State the blood parasite species.
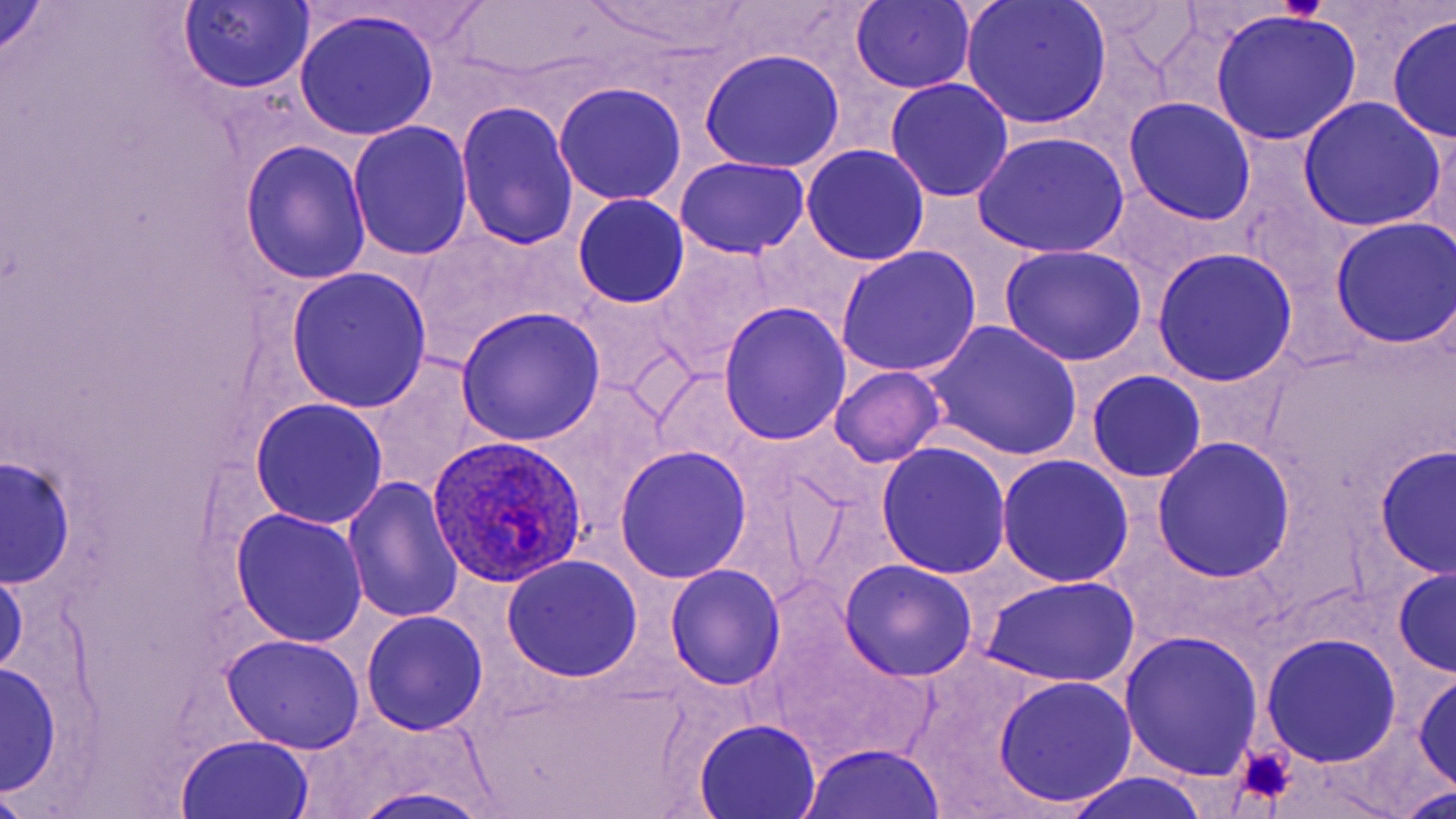

Plasmodium ovale.

Summary:
  - Coordinate format: approximate bounding boxes as named x1/y1/x2/y2 corners in pixels
  - Platelet locations: (x1=1278, y1=0, x2=1326, y2=23), (x1=1230, y1=743, x2=1299, y2=809)
  - Plasmodium ovale-infected red blood cell locations: (x1=426, y1=431, x2=589, y2=583)
  - Uninfected red blood cell locations: (x1=959, y1=0, x2=1111, y2=129), (x1=0, y1=1, x2=52, y2=65), (x1=850, y1=2, x2=975, y2=94), (x1=177, y1=3, x2=314, y2=92), (x1=295, y1=10, x2=440, y2=140), (x1=1210, y1=11, x2=1361, y2=146), (x1=1386, y1=13, x2=1456, y2=143), (x1=699, y1=48, x2=846, y2=173), (x1=886, y1=78, x2=1014, y2=202), (x1=553, y1=82, x2=687, y2=207), (x1=1298, y1=96, x2=1448, y2=230), (x1=1124, y1=97, x2=1257, y2=226), (x1=456, y1=102, x2=580, y2=253), (x1=347, y1=122, x2=474, y2=260), (x1=971, y1=131, x2=1130, y2=258), (x1=239, y1=141, x2=372, y2=286), (x1=802, y1=145, x2=929, y2=264), (x1=674, y1=155, x2=810, y2=259), (x1=572, y1=194, x2=690, y2=309), (x1=1329, y1=218, x2=1456, y2=348), (x1=652, y1=245, x2=776, y2=373), (x1=998, y1=245, x2=1147, y2=367), (x1=835, y1=246, x2=981, y2=379), (x1=1152, y1=248, x2=1298, y2=386), (x1=284, y1=267, x2=432, y2=414), (x1=719, y1=302, x2=851, y2=445), (x1=456, y1=306, x2=607, y2=448), (x1=920, y1=321, x2=1083, y2=463), (x1=360, y1=356, x2=487, y2=494), (x1=830, y1=367, x2=944, y2=467), (x1=1087, y1=369, x2=1207, y2=484), (x1=558, y1=385, x2=666, y2=494), (x1=249, y1=399, x2=389, y2=529), (x1=1152, y1=437, x2=1297, y2=582), (x1=877, y1=443, x2=1010, y2=579), (x1=614, y1=445, x2=753, y2=583), (x1=1375, y1=445, x2=1455, y2=580), (x1=3, y1=455, x2=74, y2=588), (x1=997, y1=456, x2=1132, y2=588), (x1=342, y1=477, x2=464, y2=625), (x1=231, y1=509, x2=368, y2=648), (x1=502, y1=555, x2=643, y2=683), (x1=839, y1=559, x2=978, y2=683), (x1=0, y1=564, x2=27, y2=679), (x1=665, y1=564, x2=787, y2=691), (x1=1392, y1=566, x2=1456, y2=677), (x1=981, y1=575, x2=1141, y2=690), (x1=361, y1=611, x2=490, y2=735), (x1=774, y1=623, x2=939, y2=766), (x1=1117, y1=631, x2=1266, y2=781), (x1=1260, y1=632, x2=1402, y2=769), (x1=220, y1=633, x2=366, y2=754), (x1=1, y1=662, x2=63, y2=799), (x1=1414, y1=671, x2=1455, y2=794), (x1=994, y1=676, x2=1139, y2=809), (x1=693, y1=718, x2=822, y2=818), (x1=175, y1=734, x2=315, y2=818), (x1=795, y1=743, x2=949, y2=818), (x1=1059, y1=771, x2=1211, y2=819), (x1=343, y1=781, x2=500, y2=819), (x1=0, y1=783, x2=37, y2=818), (x1=1401, y1=785, x2=1456, y2=818)
  - Preparation: thin blood film
  - Field of view: one of a larger specimen
  - Stain: May-Grünwald-Giemsa
  - Magnification: 1000x
  - Modality: light microscopy
  - Image size: 1456×819 pixels